Report the malaria status of this cell.
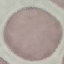
Uninfected.

Summary:
  - Capture: smartphone camera at the microscope eyepiece
  - Stain: Giemsa
  - Preparation: thin smear
  - Image type: cell patch, automatically extracted from a larger field of view and resized to 64 × 64 pixels